Describe the morphology of the red blood cells.
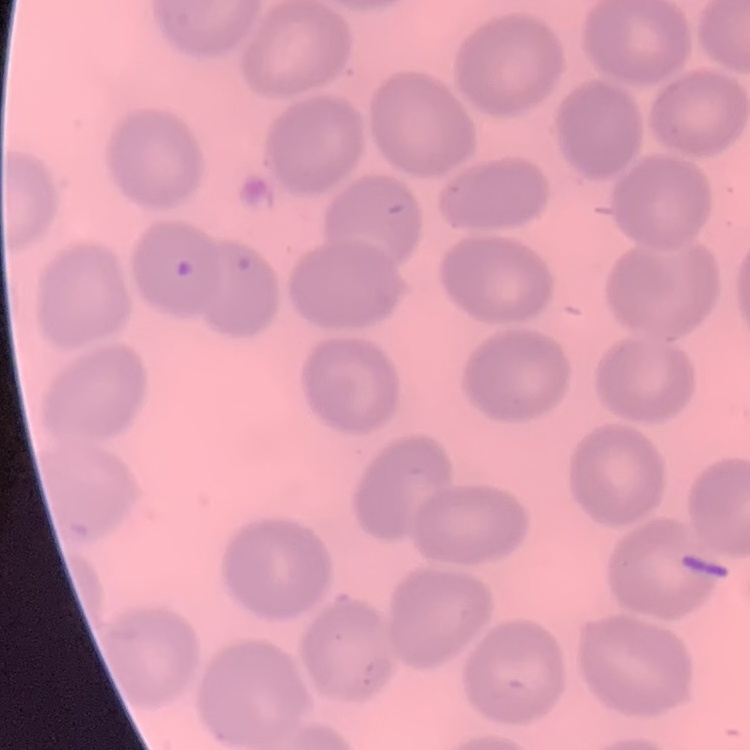

No rouleaux formation.

stain = Field's or Giemsa
preparation = thin peripheral smear
image type = square crop of a larger photomicrograph